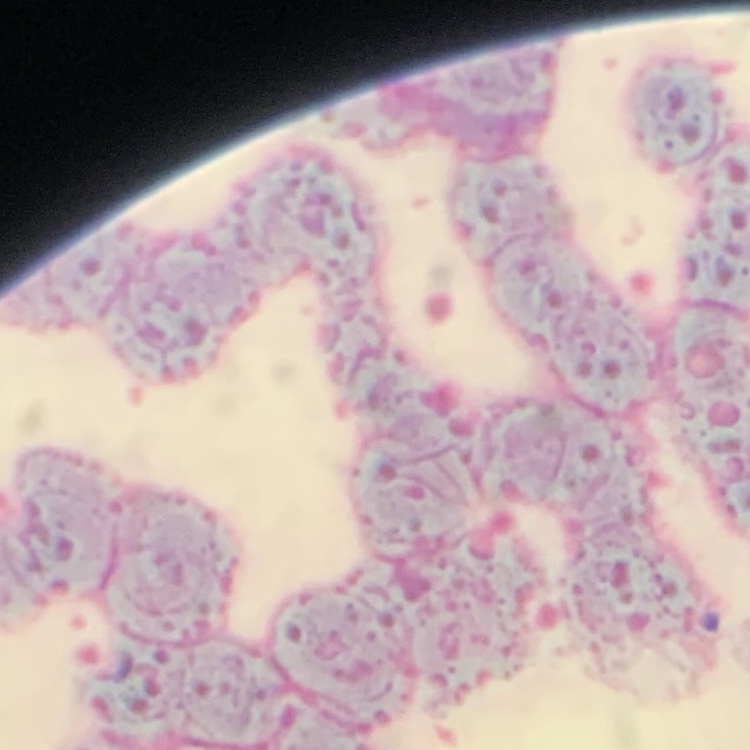 The red blood cells show rouleaux formation. Thin blood smear. Stained with either Field's or Giemsa. Square crop of a larger photomicrograph.